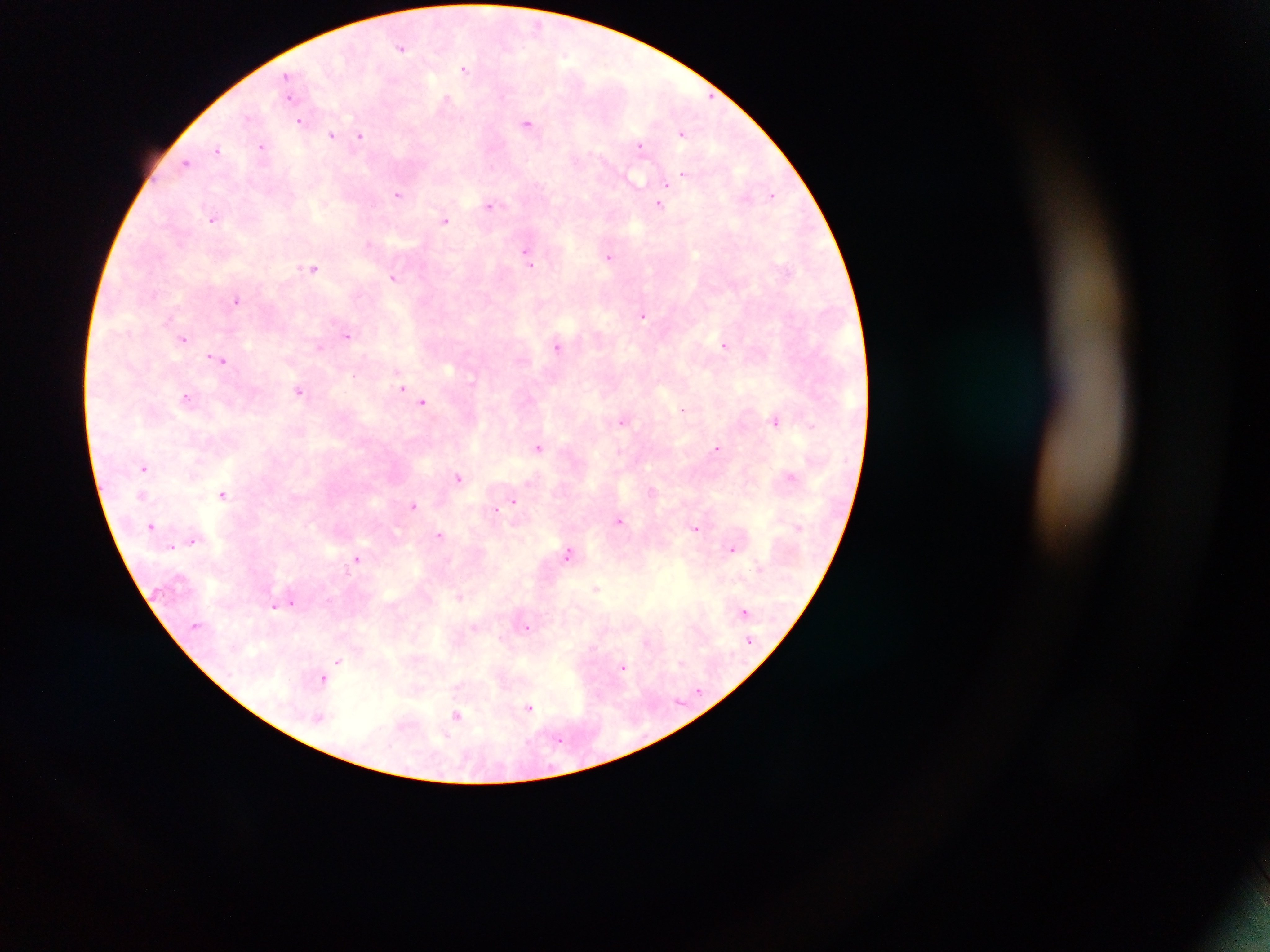
capture = mobile-phone photograph through a microscope
country = Ghana
preparation = thick blood film
image size = 1270×952 pixels
Plasmodium parasite locations = approximate centers as x y in pixels: 537 25; 402 48; 464 69; 287 76; 289 99; 445 100; 247 117; 300 121; 527 122; 682 133; 331 136; 359 136; 261 146; 640 146; 218 149; 186 163; 682 175; 635 180; 666 183; 398 193; 772 194; 659 205; 490 206; 213 219; 445 220; 368 243; 526 253; 609 256; 530 264; 313 267; 394 278; 236 300; 643 315; 347 335; 184 339; 724 345; 557 346; 319 347; 220 360; 356 375; 401 387; 299 391; 187 398; 423 402; 683 409; 622 421; 776 421; 812 426; 538 447; 717 449; 144 468; 459 477; 790 477; 222 494; 514 501; 413 505; 497 510; 620 521; 151 525; 695 528; 439 535; 192 541; 172 546; 731 549; 568 553; 356 558; 596 588; 459 597; 293 602; 274 606; 744 611; 475 627; 526 627; 339 660; 682 663; 622 668; 323 679; 529 708; 457 715; 559 739
field of view = single